Comment on the morphology of the red blood cells.
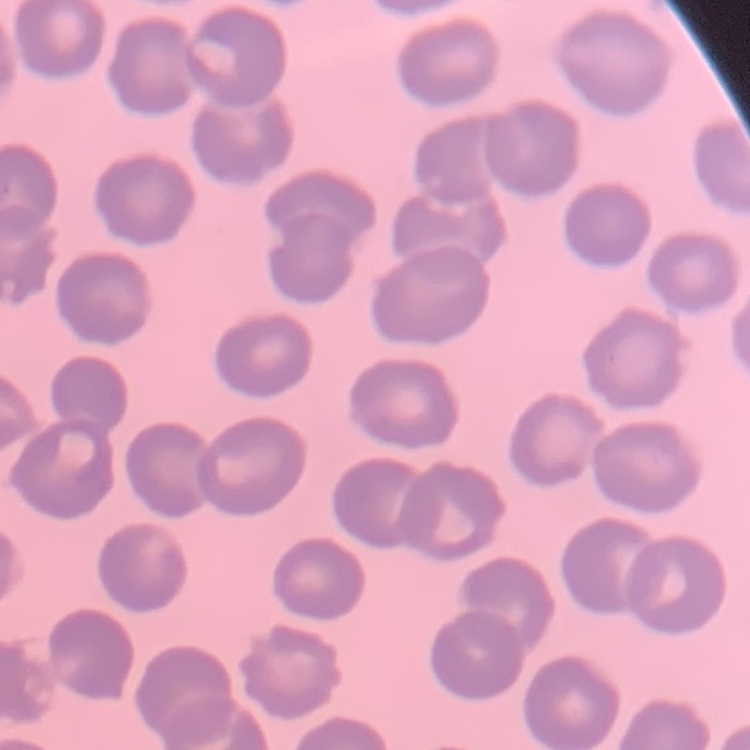
No rouleaux formation.

Thin peripheral smear. Field's or Giemsa stain. Square crop of a larger photomicrograph.